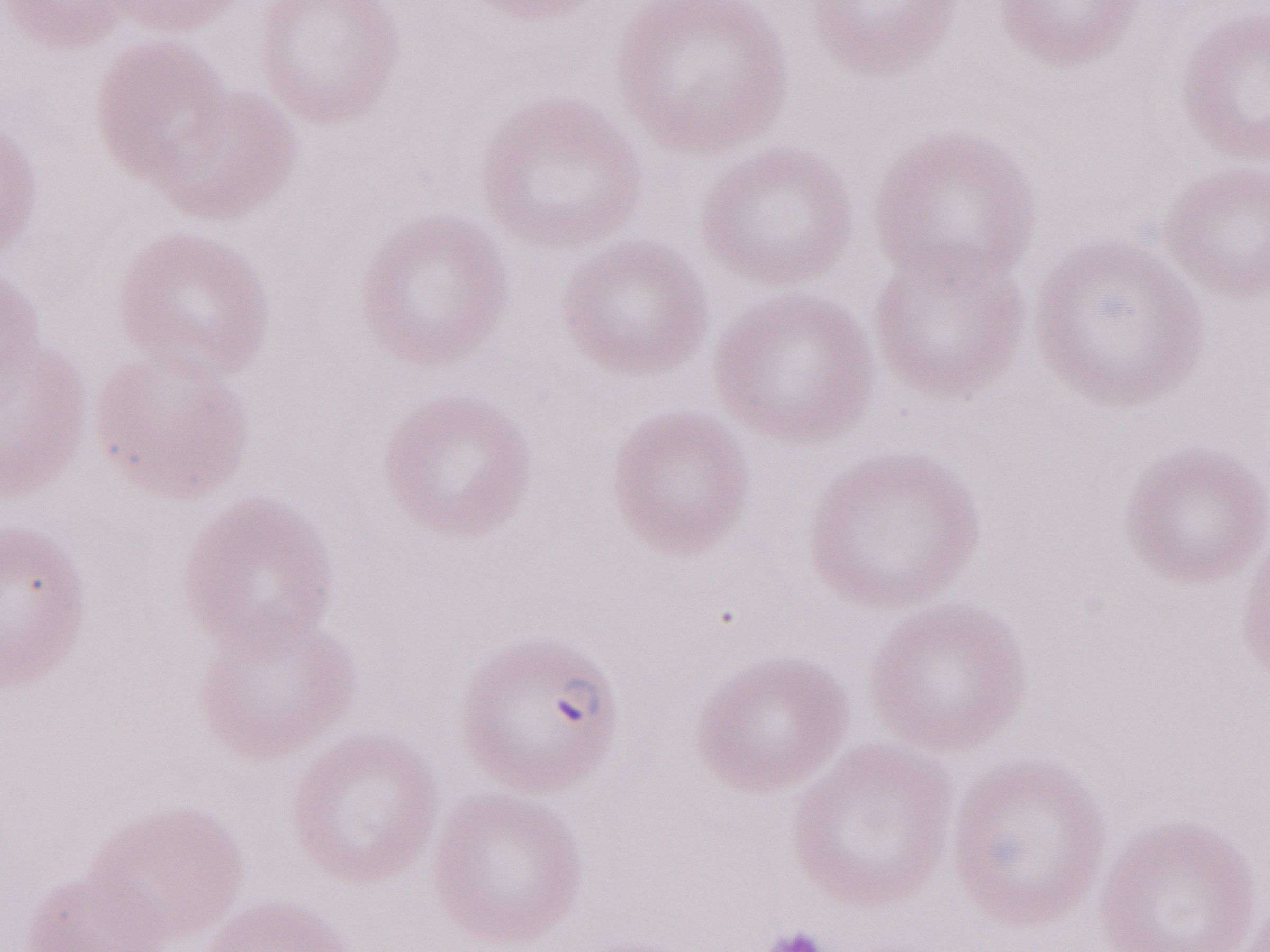
Magnification: 1,000x. Patient-level malaria diagnosis: positive. One field of this slide. Thin blood smear. May-Grünwald-Giemsa-stained preparation. Olympus BX43 microscope, Olympus DP73 camera. Image is 1270×952 pixels.